Report the malaria status of this cell.
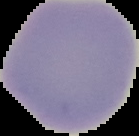

Uninfected.

image_size: 139×136 pixels
preparation: thin blood smear
image_type: segmented cell region on a black background